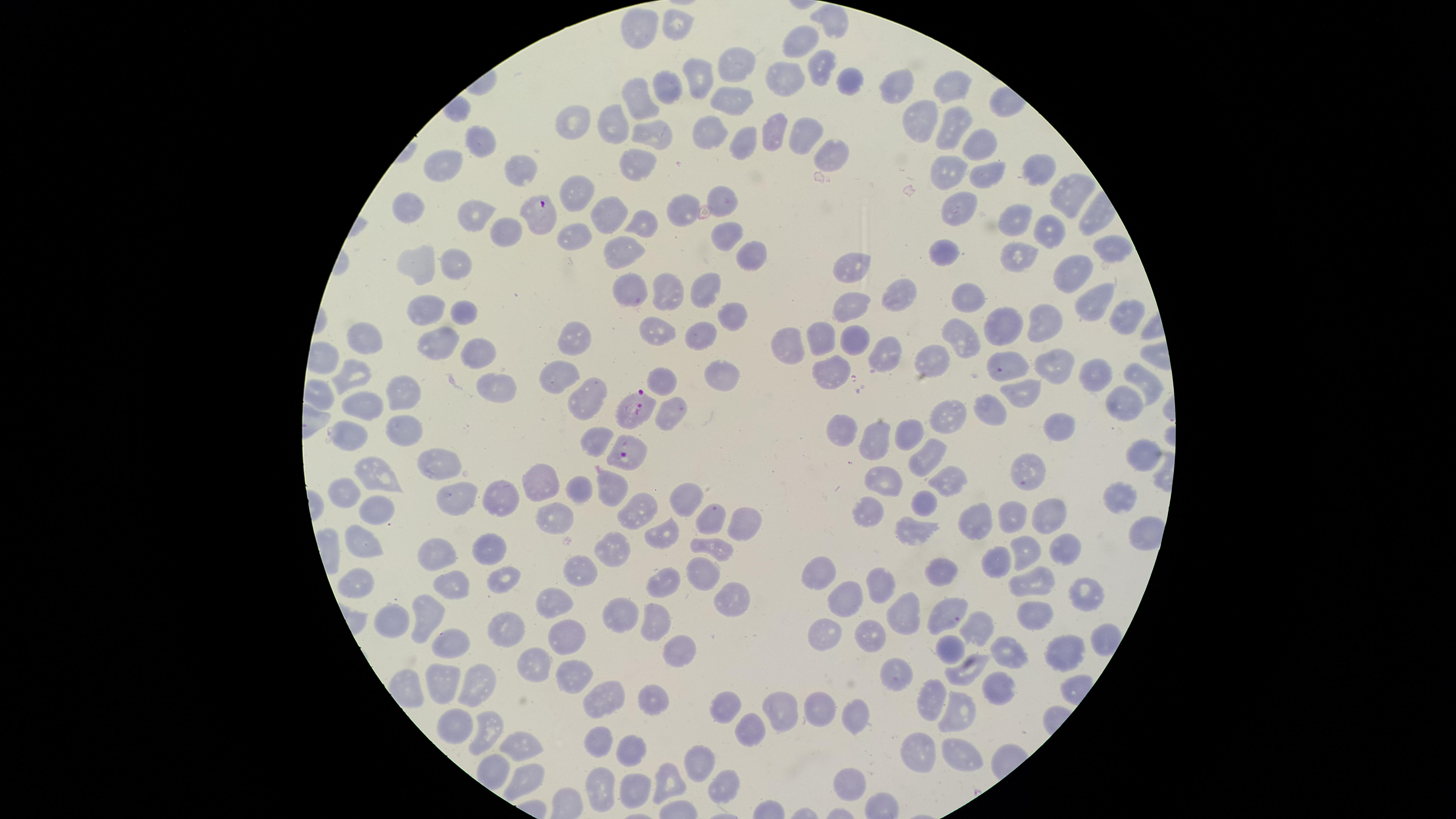
presence = malaria parasites identified
capture = smartphone photograph through the microscope eyepiece
stain = Giemsa
uninfected red blood cells = approximate marker points as (x, y) in pixels: (831, 21), (672, 23), (637, 29), (801, 46), (732, 67), (819, 67), (698, 74), (781, 81), (842, 81), (901, 81), (952, 84), (658, 88), (728, 97), (639, 106), (609, 121), (923, 122), (950, 124), (572, 127), (799, 128), (711, 131), (770, 131), (650, 135), (742, 137), (477, 141), (977, 142), (828, 150), (446, 165), (633, 165), (515, 168), (942, 171), (982, 171), (1038, 171), (722, 195), (1064, 195), (574, 198), (685, 203), (954, 206), (409, 213), (607, 213), (471, 215), (1023, 218), (639, 222), (1049, 229), (571, 233), (503, 234), (728, 236), (1110, 244), (623, 250), (952, 253), (1023, 253), (751, 255), (452, 263), (416, 265), (853, 268), (1066, 274), (634, 283), (709, 289), (666, 293), (972, 293), (904, 299), (1090, 301), (425, 308), (844, 308), (461, 310), (1120, 311), (732, 315), (1000, 318), (1048, 318), (653, 327), (702, 331), (962, 333), (819, 334), (365, 338), (786, 338), (854, 339), (572, 341), (441, 344), (883, 349), (928, 356), (476, 357), (1050, 357), (1005, 359), (832, 366), (357, 370), (1084, 370), (1142, 374), (556, 375), (662, 376), (719, 377), (492, 383), (403, 394), (1024, 395), (584, 401), (1124, 403), (990, 407), (366, 408), (671, 413), (948, 413), (1061, 419), (850, 426), (403, 430), (913, 433), (880, 434), (593, 442), (1141, 453), (926, 454), (436, 459), (1032, 463), (372, 472), (881, 472), (948, 472), (544, 481), (610, 489), (344, 490), (579, 490), (683, 496), (1117, 496), (461, 500), (505, 500), (925, 502), (379, 508), (637, 510), (552, 513), (714, 513), (872, 514), (1048, 515), (1019, 516), (744, 517), (985, 520), (912, 529), (661, 531), (1144, 532), (357, 542), (709, 546), (1021, 546), (1062, 546), (608, 551), (435, 552), (491, 554), (993, 554), (941, 569), (703, 570), (584, 571), (824, 571), (666, 577), (1038, 577), (504, 578), (357, 580), (878, 583), (454, 585), (1084, 592), (728, 594), (848, 599), (549, 600), (943, 612), (626, 613), (430, 614), (908, 614), (402, 615), (1040, 615), (653, 620), (978, 623), (824, 628), (571, 633), (503, 634), (868, 636), (448, 645), (947, 646), (1068, 646), (680, 649), (1001, 650), (531, 661), (970, 666), (898, 671), (578, 676), (439, 683), (1004, 683), (472, 687), (608, 694), (935, 697), (652, 698), (725, 704), (785, 706), (819, 706), (959, 708), (849, 719), (449, 723), (749, 727), (484, 730), (597, 737), (517, 747), (959, 747), (632, 748), (916, 750), (695, 762), (534, 776), (847, 781), (632, 783), (670, 783), (724, 785), (602, 786)
preparation = thin blood film
species = Plasmodium falciparum
field of view = single
visible region = circular
image size = 1456×819 pixels
parasitized red blood cells = approximate marker points as (x, y) in pixels: (544, 220), (632, 407), (348, 433), (631, 450)